Locate every blood parasite and identify its species.
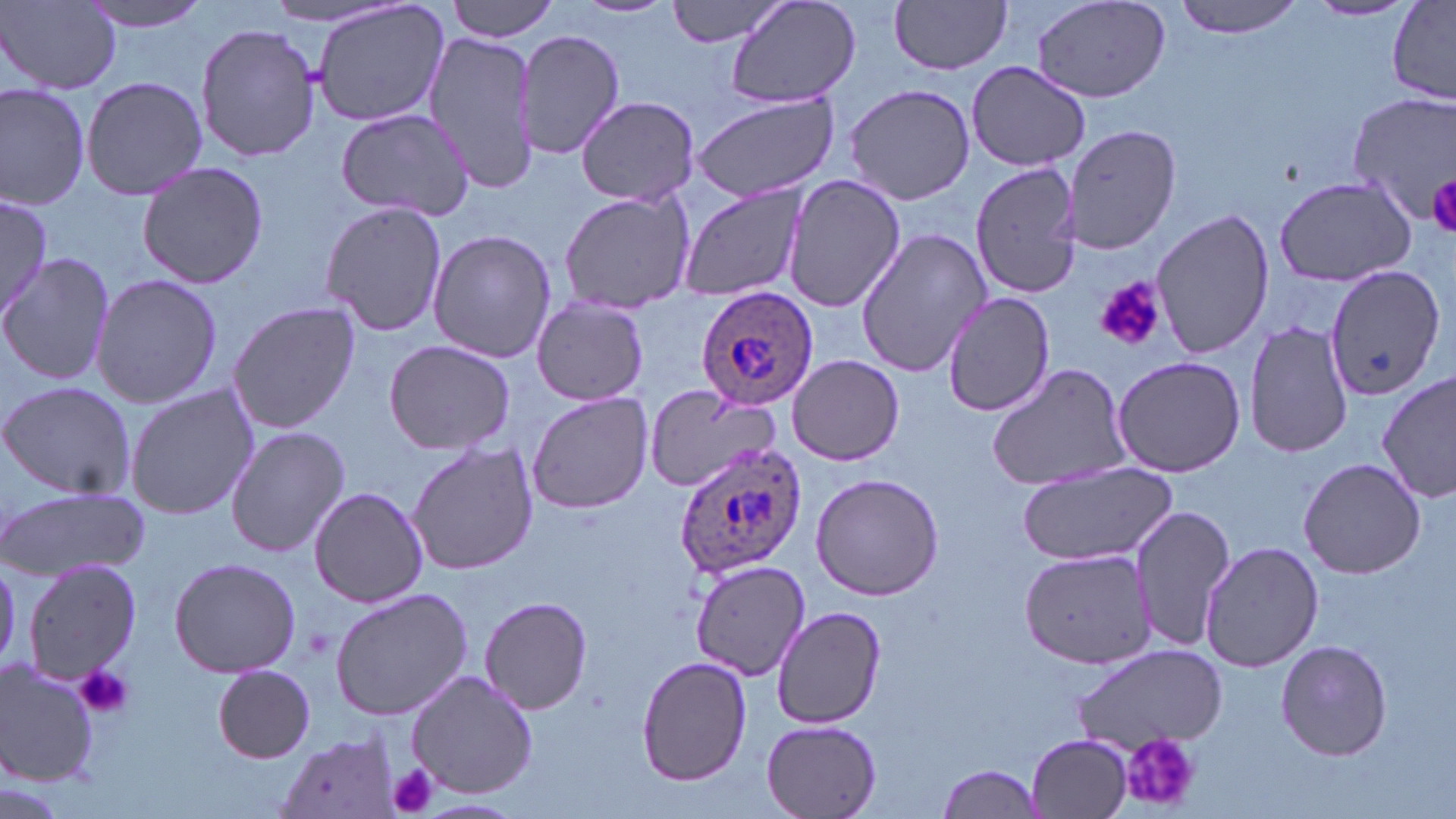

Approximate bounding boxes as (x1, y1, x2, y2) in pixels.
Plasmodium ovale-infected red blood cells: (696, 285, 820, 408), (671, 440, 806, 579).
No Plasmodium falciparum, Plasmodium malariae, Plasmodium vivax, Babesia divergens, or Trypanosoma brucei observed.

slide-level diagnosis = Plasmodium ovale
preparation = thin blood smear
field of view = one of a larger specimen
stain = May-Grünwald-Giemsa
uninfected red blood cell locations = approximate bounding boxes as (x1, y1, x2, y2) in pixels: (81, 0, 218, 33), (258, 0, 411, 33), (446, 0, 560, 41), (572, 0, 679, 21), (662, 0, 794, 47), (725, 0, 862, 111), (1170, 0, 1311, 38), (1387, 0, 1456, 102), (2, 1, 120, 94), (311, 1, 450, 131), (890, 1, 1015, 75), (1028, 1, 1172, 104), (1307, 1, 1416, 22), (195, 21, 320, 164), (516, 29, 625, 160), (424, 32, 542, 193), (964, 62, 1091, 172), (80, 75, 208, 201), (0, 83, 90, 210), (841, 83, 979, 206), (1346, 91, 1456, 225), (689, 94, 840, 204), (576, 96, 699, 206), (334, 106, 478, 223), (1062, 124, 1181, 253), (973, 161, 1084, 296), (136, 162, 268, 288), (781, 173, 905, 315), (1273, 175, 1418, 287), (675, 182, 811, 305), (556, 189, 697, 316), (0, 193, 52, 328), (318, 200, 448, 340), (1150, 207, 1274, 360), (855, 227, 992, 377), (428, 229, 556, 364), (1, 253, 114, 387), (1322, 264, 1446, 403), (90, 273, 223, 410), (942, 290, 1056, 418), (531, 296, 652, 407), (227, 302, 360, 435), (1244, 320, 1353, 459), (382, 339, 515, 456), (788, 355, 905, 464), (1110, 355, 1246, 477), (986, 362, 1133, 494), (1377, 371, 1455, 504), (0, 380, 135, 499), (125, 382, 260, 521), (646, 385, 780, 493), (525, 390, 656, 515), (225, 425, 350, 557), (406, 441, 539, 576), (1298, 459, 1428, 577), (1016, 460, 1178, 566), (811, 473, 946, 600), (1, 485, 151, 580), (310, 487, 430, 607), (1131, 504, 1234, 655), (1201, 540, 1323, 673), (1017, 546, 1158, 670), (168, 556, 301, 679), (689, 557, 809, 679), (22, 558, 146, 685), (329, 587, 474, 722), (479, 595, 594, 715), (772, 606, 885, 728), (1275, 640, 1392, 762), (1073, 646, 1229, 753), (636, 655, 752, 788), (1, 659, 102, 786), (211, 666, 317, 763), (404, 669, 537, 797), (760, 717, 885, 819), (275, 732, 402, 818), (1027, 734, 1133, 817), (937, 763, 1045, 816), (412, 796, 527, 818)
modality = optical microscopy
image size = 1456×819 pixels
platelet locations = approximate bounding boxes as (x1, y1, x2, y2) in pixels: (1427, 173, 1456, 238), (1095, 276, 1164, 352), (76, 663, 132, 720), (1119, 733, 1200, 808), (387, 762, 441, 816)
magnification = 1000x